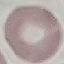
Summary:
  - Result: no malaria parasites detected
  - Preparation: thin blood film
  - Image type: automatically extracted cell patch, resized to 64 × 64 pixels
  - Capture: smartphone camera at the microscope eyepiece
  - Stain: Giemsa